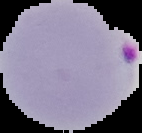

Image is 142×133 pixels. From a thin blood smear. The area outside the segmented cell region is set to black. Result: malaria parasites detected.